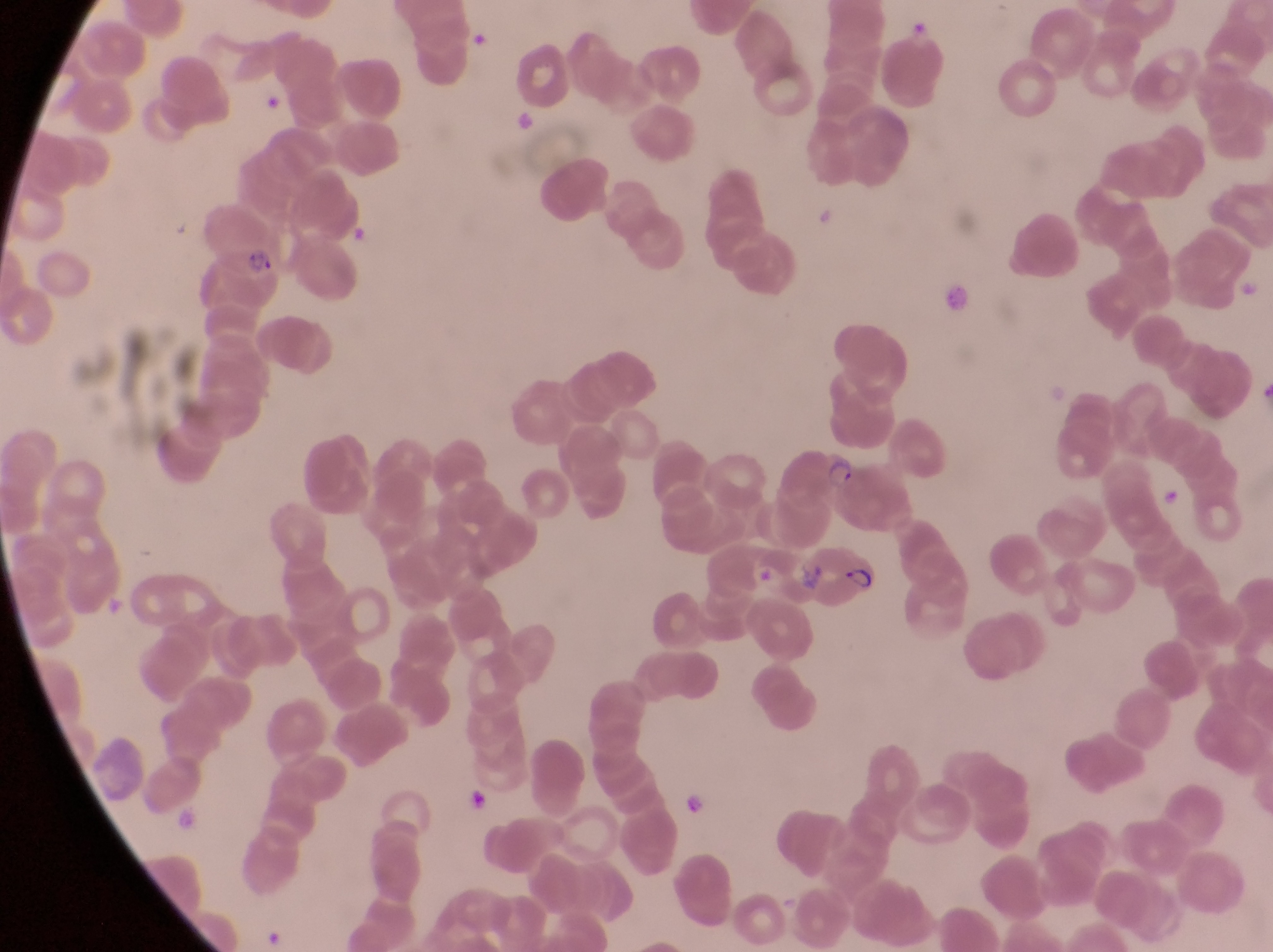
Approximate bounding boxes as left top right bottom in pixels.
Summary:
  - Artifact (platelet-like body, stain precipitate, or debris) locations: 266 93 292 120; 511 107 544 137; 942 283 974 314; 943 283 998 335; 469 789 492 813; 682 793 706 820
  - Parasitised red blood cell locations: 195 197 287 290; 784 437 867 519; 808 540 883 615
  - Leukocyte locations: 470 27 489 47
  - Capture: smartphone photograph through the eyepiece of an Olympus CX-23 microscope
  - Country: Uganda
  - Magnification: 1000x
  - Preparation: thin blood smear
  - Field of view: single
  - Image size: 1273×952 pixels